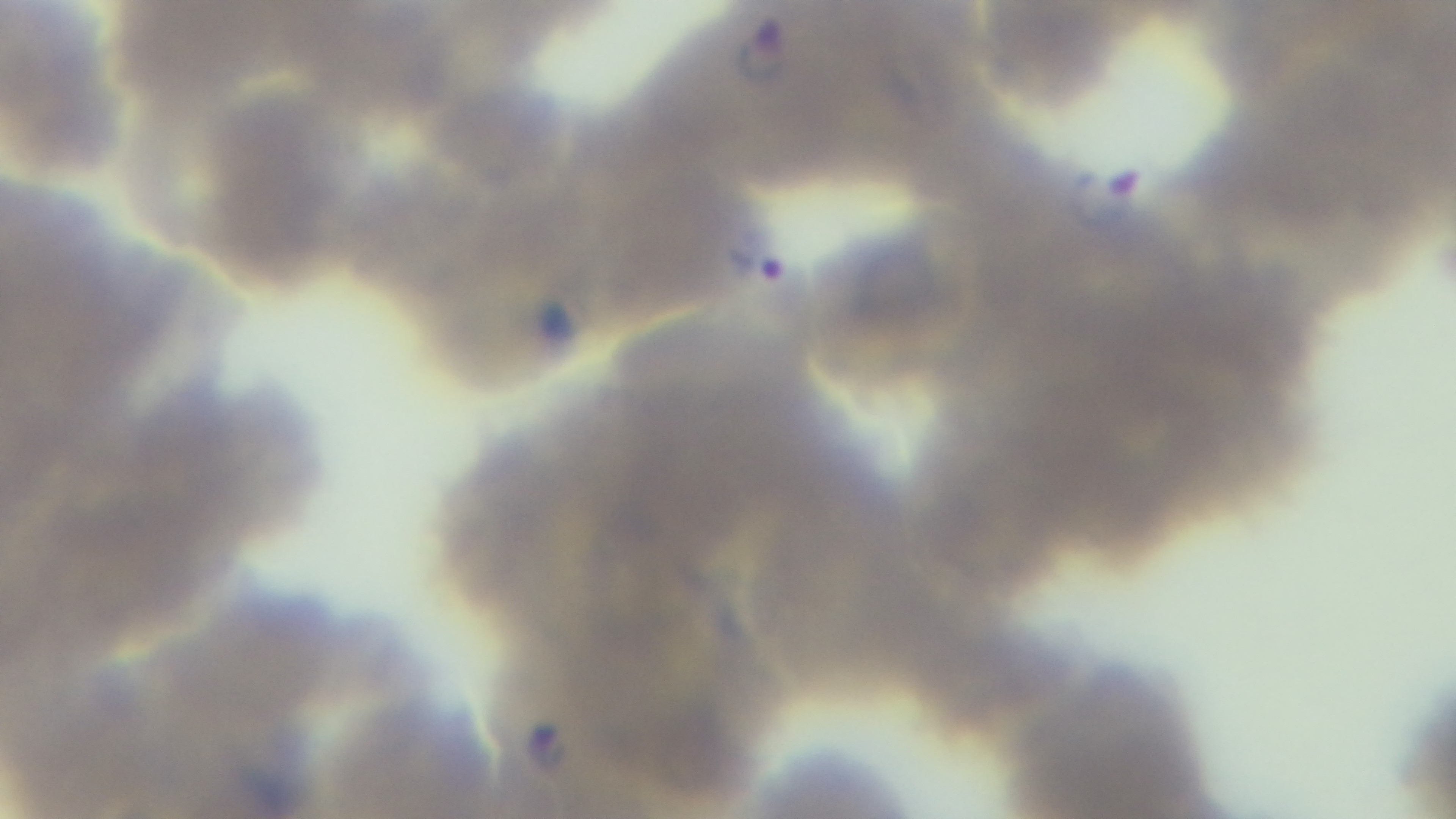

100x oil-immersion objective. Malaria status: infected. Light microscopy. One field from the slide. Giemsa-stained. Preparation: thin. Captured with a mounted 4K digital camera.